Assess this cell for malaria.
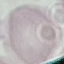
It is uninfected.

Cell patch, automatically extracted from a larger field of view and resized to 64 × 64 pixels. Thin blood smear. Acquired by smartphone through the microscope eyepiece. Giemsa-stained preparation.